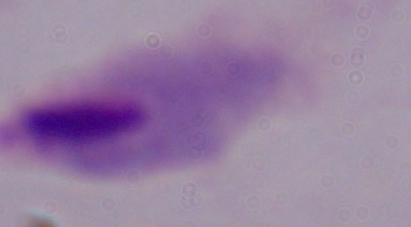
1000x magnification. A trichomonad is seen. Micrograph.